Comment on the morphology of the erythrocytes.
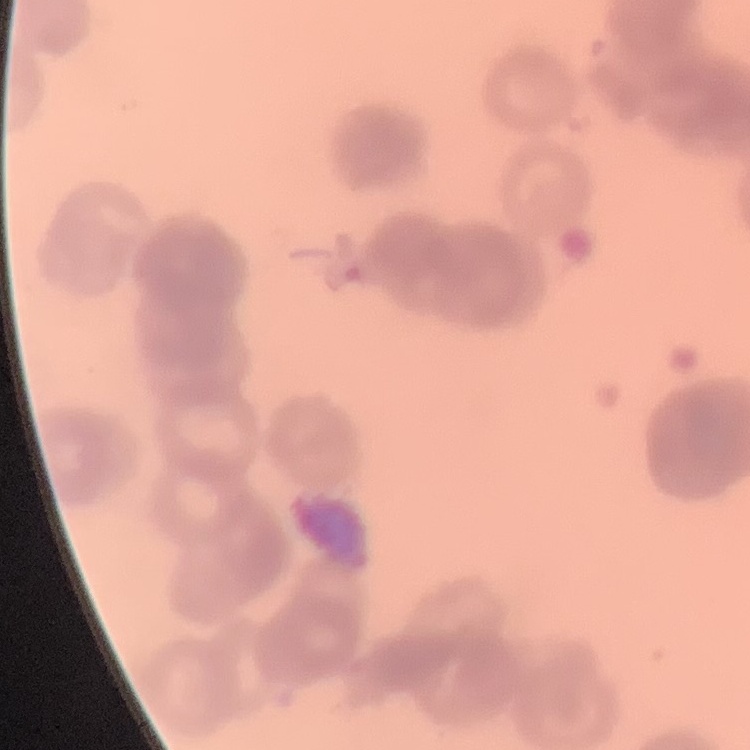

Rouleaux formation.

stain = Field's or Giemsa
preparation = thin peripheral smear
image type = square crop of a larger photomicrograph